Assess this cell for malaria.
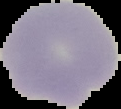

Uninfected.

image type = segmented cell region on a black background
preparation = thin blood film
image size = 121×109 pixels